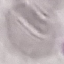 Result: negative for malaria parasites. Photographed with a smartphone camera at the microscope eyepiece. Thin blood smear. Automatically extracted cell patch, resized to 64 × 64 pixels. Giemsa-stained preparation.